Assess this cell for malaria.
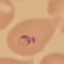
Parasitized.

Thin smear of blood. Automatically extracted cell patch, resized to 64 × 64 pixels. Photographed with a smartphone camera at the microscope eyepiece. Giemsa stain.